Classify this cell by malaria status.
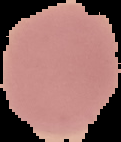

Uninfected.

From a thin blood smear. The area outside the segmented cell region is set to black. Image is 121×142 pixels.